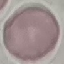

result: no malaria parasites seen
preparation: thin blood film
capture: smartphone through the microscope eyepiece
stain: Giemsa
image_type: automatically extracted cell patch, resized to 64 × 64 pixels